Identify the parasite.
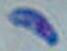

This is Toxoplasma gondii.

modality = micrograph
magnification = 1000x